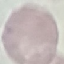
Malaria status: uninfected. Thin blood smear. Automatically extracted cell patch, resized to 64 × 64 pixels. Giemsa-stained preparation. Photographed with a smartphone camera at the microscope eyepiece.